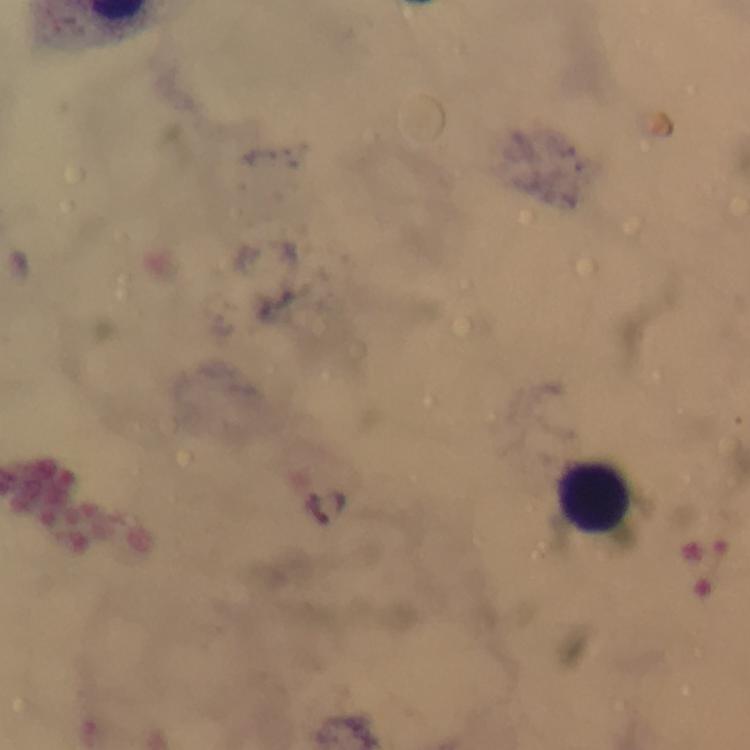

Approximate object centers, in pixels from the top-left corner.
Summary:
  - Leukocyte locations: (x=594, y=496)
  - Capture: smartphone mounted on the microscope
  - Malaria parasites: none seen
  - Image size: 750×750 pixels
  - Preparation: thick smear
  - Cropped from: one field of view
  - Context: from a malaria diagnostic workup
  - Stain: Giemsa
  - Immersion oil: used
  - Magnification: 100x